Give the extent of all Plasmodium malariae-infected red blood cells.
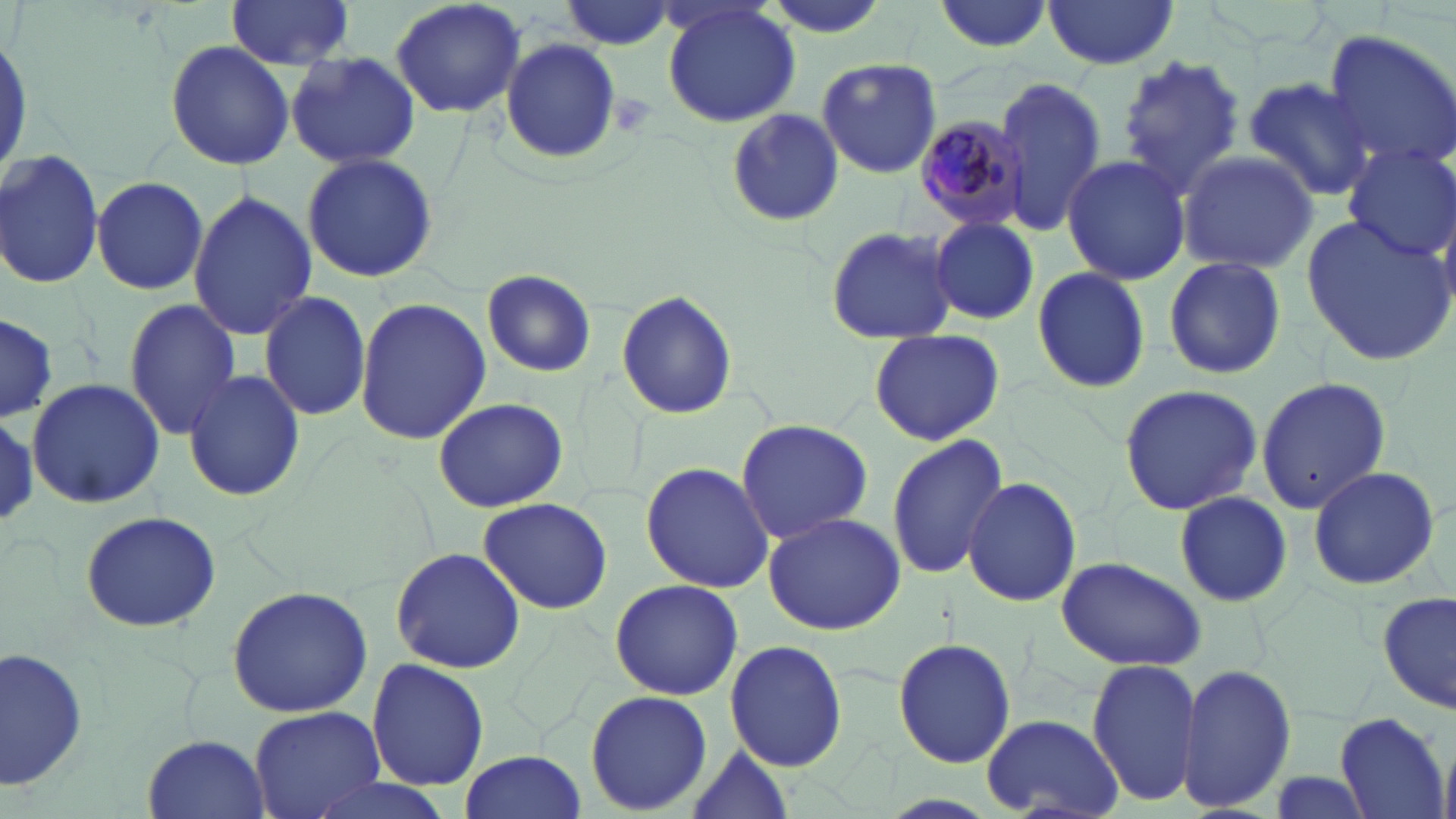
Approximate bounding boxes as named x1/y1/x2/y2 corners in pixels.
Plasmodium malariae-infected red blood cells: (x1=912, y1=109, x2=1029, y2=238).

{
  "slide_level_diagnosis": "Plasmodium malariae",
  "field_of_view": "one of a larger specimen",
  "preparation": "thin blood smear",
  "image_size": "1456×819 pixels",
  "stain": "May-Grünwald-Giemsa",
  "uninfected_red_blood_cell_locations": "approximate bounding boxes as named x1/y1/x2/y2 corners in pixels: (x1=224, y1=0, x2=357, y2=71), (x1=389, y1=0, x2=528, y2=118), (x1=932, y1=0, x2=1056, y2=53), (x1=1042, y1=0, x2=1179, y2=69), (x1=559, y1=1, x2=677, y2=49), (x1=660, y1=2, x2=802, y2=128), (x1=1319, y1=29, x2=1456, y2=173), (x1=500, y1=36, x2=620, y2=163), (x1=164, y1=41, x2=296, y2=172), (x1=285, y1=51, x2=420, y2=170), (x1=1116, y1=53, x2=1247, y2=196), (x1=814, y1=59, x2=944, y2=178), (x1=990, y1=77, x2=1105, y2=236), (x1=1242, y1=77, x2=1376, y2=201), (x1=1026, y1=95, x2=1177, y2=262), (x1=726, y1=108, x2=842, y2=226), (x1=1342, y1=146, x2=1456, y2=260), (x1=0, y1=150, x2=103, y2=289), (x1=1176, y1=150, x2=1317, y2=274), (x1=1061, y1=153, x2=1191, y2=284), (x1=300, y1=154, x2=440, y2=284), (x1=90, y1=176, x2=209, y2=296), (x1=188, y1=190, x2=318, y2=341), (x1=1299, y1=214, x2=1456, y2=365), (x1=928, y1=217, x2=1041, y2=324), (x1=824, y1=226, x2=960, y2=345), (x1=1160, y1=256, x2=1288, y2=379), (x1=1029, y1=266, x2=1151, y2=393), (x1=482, y1=269, x2=596, y2=379), (x1=259, y1=289, x2=372, y2=424), (x1=617, y1=289, x2=740, y2=420), (x1=355, y1=296, x2=489, y2=445), (x1=121, y1=299, x2=242, y2=439), (x1=0, y1=310, x2=58, y2=423), (x1=866, y1=329, x2=1006, y2=446), (x1=182, y1=369, x2=306, y2=502), (x1=1256, y1=376, x2=1391, y2=512), (x1=25, y1=379, x2=164, y2=507), (x1=1118, y1=383, x2=1263, y2=516), (x1=432, y1=396, x2=569, y2=513), (x1=0, y1=409, x2=37, y2=528), (x1=734, y1=419, x2=874, y2=542), (x1=885, y1=432, x2=1011, y2=582), (x1=640, y1=461, x2=774, y2=594), (x1=1305, y1=466, x2=1443, y2=592), (x1=963, y1=476, x2=1083, y2=609), (x1=1173, y1=491, x2=1294, y2=608), (x1=477, y1=496, x2=614, y2=614), (x1=79, y1=510, x2=222, y2=632), (x1=761, y1=511, x2=906, y2=636), (x1=390, y1=546, x2=525, y2=675), (x1=1055, y1=556, x2=1206, y2=672), (x1=609, y1=578, x2=743, y2=701), (x1=226, y1=586, x2=373, y2=718), (x1=1380, y1=590, x2=1455, y2=717), (x1=892, y1=636, x2=1017, y2=768), (x1=725, y1=640, x2=847, y2=771), (x1=1, y1=645, x2=94, y2=798), (x1=366, y1=658, x2=491, y2=793), (x1=1086, y1=658, x2=1203, y2=807), (x1=1175, y1=662, x2=1300, y2=811), (x1=583, y1=688, x2=712, y2=816), (x1=250, y1=705, x2=388, y2=819), (x1=1335, y1=712, x2=1448, y2=818), (x1=980, y1=713, x2=1124, y2=818), (x1=143, y1=732, x2=267, y2=817), (x1=682, y1=743, x2=796, y2=819), (x1=459, y1=749, x2=587, y2=817), (x1=1261, y1=772, x2=1380, y2=817), (x1=296, y1=776, x2=459, y2=819)",
  "modality": "light microscopy",
  "magnification": "1000x"
}